Assess this cell for malaria.
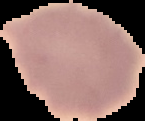
It is uninfected.

preparation = thin blood smear
image type = cell region segmented out of the field of view; surrounding area masked to black
image size = 145×121 pixels